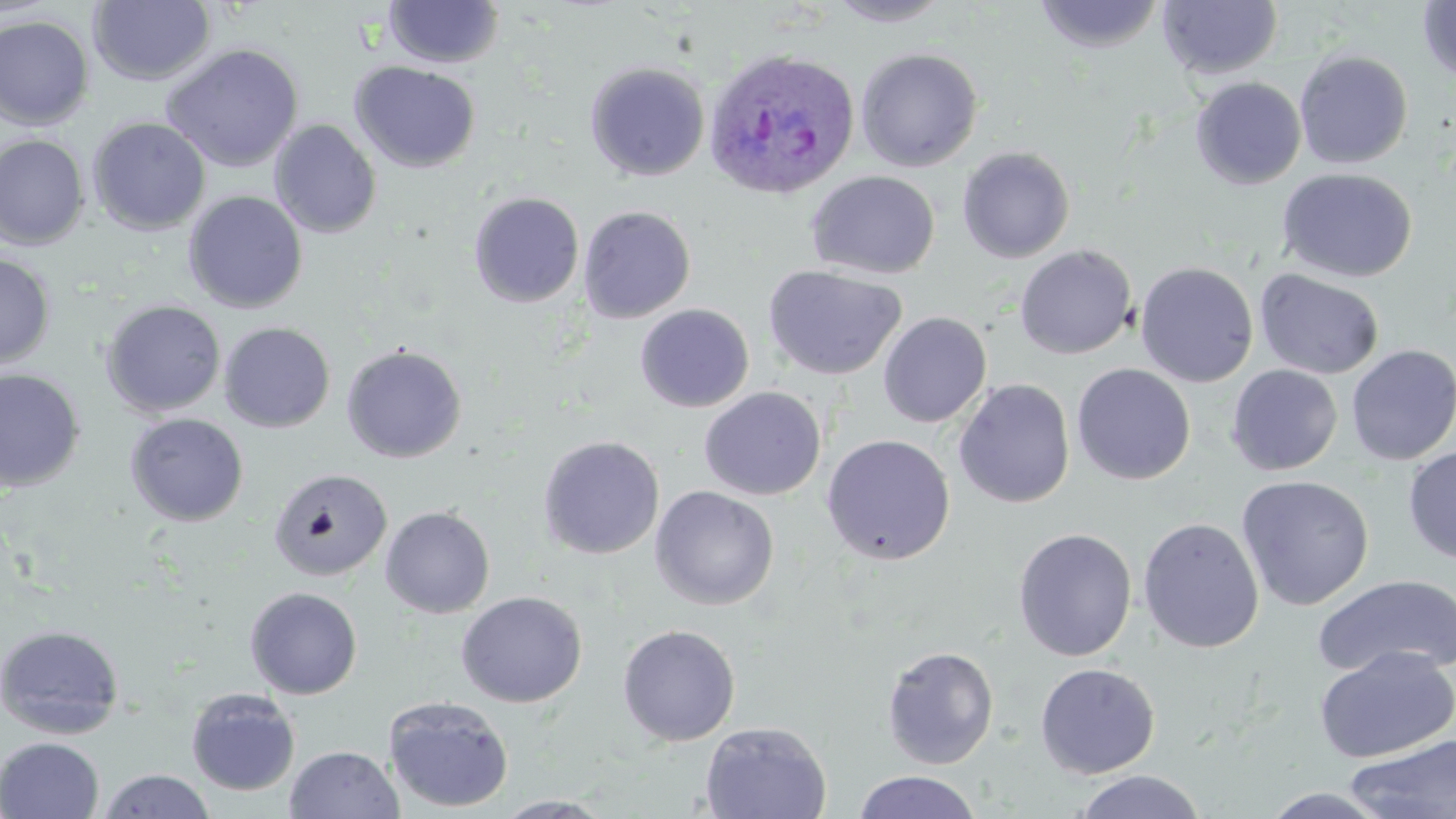

Approximate bounding boxes as named x1/y1/x2/y2 corners in pixels. Uninfected red blood cell locations: (x1=825, y1=0, x2=955, y2=27), (x1=1033, y1=0, x2=1165, y2=53), (x1=88, y1=1, x2=216, y2=86), (x1=383, y1=1, x2=505, y2=69), (x1=1158, y1=1, x2=1283, y2=80), (x1=1417, y1=1, x2=1456, y2=85), (x1=0, y1=14, x2=95, y2=130), (x1=160, y1=43, x2=304, y2=173), (x1=856, y1=47, x2=983, y2=172), (x1=1294, y1=50, x2=1413, y2=169), (x1=349, y1=61, x2=481, y2=173), (x1=584, y1=61, x2=711, y2=181), (x1=1190, y1=77, x2=1307, y2=190), (x1=88, y1=117, x2=211, y2=236), (x1=269, y1=120, x2=382, y2=238), (x1=0, y1=134, x2=89, y2=250), (x1=957, y1=146, x2=1075, y2=263), (x1=1277, y1=167, x2=1418, y2=283), (x1=806, y1=170, x2=940, y2=279), (x1=183, y1=190, x2=308, y2=314), (x1=468, y1=192, x2=584, y2=307), (x1=578, y1=205, x2=696, y2=324), (x1=1014, y1=244, x2=1138, y2=360), (x1=0, y1=253, x2=56, y2=368), (x1=1135, y1=261, x2=1259, y2=387), (x1=762, y1=264, x2=907, y2=380), (x1=1254, y1=268, x2=1385, y2=381), (x1=100, y1=300, x2=226, y2=417), (x1=635, y1=303, x2=755, y2=412), (x1=878, y1=311, x2=992, y2=428), (x1=219, y1=322, x2=336, y2=433), (x1=341, y1=344, x2=467, y2=463), (x1=1345, y1=344, x2=1456, y2=465), (x1=1071, y1=363, x2=1196, y2=485), (x1=1226, y1=364, x2=1343, y2=476), (x1=0, y1=368, x2=85, y2=492), (x1=954, y1=378, x2=1075, y2=509), (x1=700, y1=387, x2=826, y2=500), (x1=125, y1=413, x2=249, y2=527), (x1=821, y1=433, x2=956, y2=565), (x1=537, y1=435, x2=665, y2=560), (x1=1403, y1=445, x2=1456, y2=564), (x1=268, y1=467, x2=392, y2=581), (x1=1236, y1=475, x2=1375, y2=611), (x1=649, y1=486, x2=779, y2=610), (x1=380, y1=506, x2=495, y2=618), (x1=1138, y1=517, x2=1264, y2=654), (x1=1013, y1=528, x2=1137, y2=661), (x1=1310, y1=574, x2=1456, y2=680), (x1=244, y1=587, x2=363, y2=699), (x1=456, y1=591, x2=588, y2=708), (x1=0, y1=624, x2=125, y2=739), (x1=618, y1=624, x2=740, y2=746), (x1=882, y1=646, x2=999, y2=769), (x1=1314, y1=646, x2=1456, y2=763), (x1=1035, y1=663, x2=1161, y2=780), (x1=186, y1=688, x2=301, y2=796), (x1=384, y1=696, x2=514, y2=813), (x1=699, y1=722, x2=832, y2=819), (x1=1346, y1=734, x2=1456, y2=818), (x1=0, y1=737, x2=104, y2=819), (x1=285, y1=745, x2=404, y2=818), (x1=97, y1=769, x2=216, y2=819), (x1=852, y1=770, x2=983, y2=819), (x1=1071, y1=770, x2=1208, y2=819), (x1=1259, y1=787, x2=1397, y2=818), (x1=493, y1=795, x2=616, y2=818). Plasmodium ovale-infected red blood cell locations: (x1=702, y1=47, x2=860, y2=200). Slide-level diagnosis: Plasmodium ovale. Captured at 1000x magnification. Thin blood film. Image is 1456×819 pixels. One field of a larger specimen. May-Grünwald-Giemsa-stained preparation. Light microscopy.